Locate and identify every blood parasite.
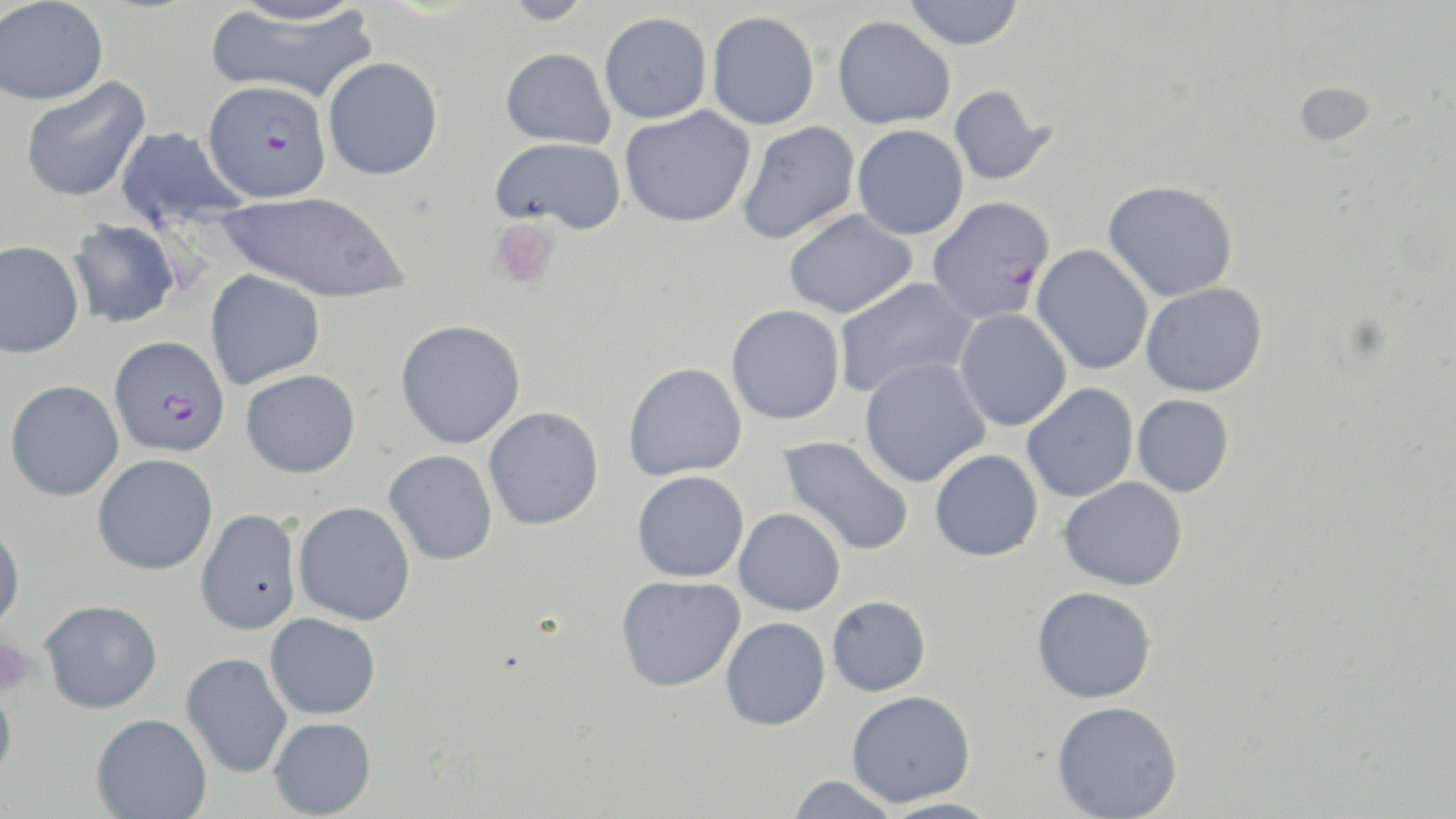
Approximate bounding boxes as named x1/y1/x2/y2 corners in pixels.
Plasmodium falciparum-infected red blood cells: (x1=203, y1=80, x2=332, y2=202), (x1=927, y1=196, x2=1056, y2=323), (x1=109, y1=335, x2=230, y2=456).
No Plasmodium ovale, Plasmodium malariae, Plasmodium vivax, Babesia divergens, or Trypanosoma brucei observed.

slide-level diagnosis = Plasmodium falciparum
platelet locations = approximate bounding boxes as named x1/y1/x2/y2 corners in pixels: (x1=488, y1=218, x2=561, y2=290), (x1=0, y1=637, x2=36, y2=701)
preparation = thin blood film
image size = 1456×819 pixels
field of view = single
modality = light microscopy
magnification = 1000x
uninfected red blood cell locations = approximate bounding boxes as named x1/y1/x2/y2 corners in pixels: (x1=500, y1=0, x2=598, y2=25), (x1=902, y1=0, x2=1025, y2=50), (x1=0, y1=1, x2=109, y2=106), (x1=225, y1=1, x2=372, y2=26), (x1=205, y1=4, x2=379, y2=104), (x1=707, y1=10, x2=820, y2=130), (x1=599, y1=12, x2=712, y2=124), (x1=832, y1=15, x2=956, y2=129), (x1=500, y1=48, x2=616, y2=148), (x1=322, y1=57, x2=443, y2=180), (x1=19, y1=76, x2=151, y2=203), (x1=1294, y1=82, x2=1375, y2=146), (x1=949, y1=84, x2=1054, y2=186), (x1=619, y1=105, x2=756, y2=228), (x1=736, y1=121, x2=860, y2=245), (x1=852, y1=124, x2=969, y2=241), (x1=114, y1=126, x2=247, y2=229), (x1=490, y1=136, x2=626, y2=233), (x1=1103, y1=180, x2=1239, y2=303), (x1=219, y1=190, x2=409, y2=303), (x1=783, y1=209, x2=918, y2=319), (x1=67, y1=219, x2=181, y2=329), (x1=0, y1=239, x2=84, y2=358), (x1=1031, y1=245, x2=1154, y2=375), (x1=205, y1=269, x2=326, y2=389), (x1=832, y1=276, x2=977, y2=399), (x1=1141, y1=282, x2=1267, y2=397), (x1=726, y1=304, x2=845, y2=425), (x1=954, y1=309, x2=1072, y2=432), (x1=395, y1=319, x2=526, y2=449), (x1=859, y1=357, x2=991, y2=487), (x1=622, y1=363, x2=748, y2=481), (x1=240, y1=369, x2=361, y2=478), (x1=4, y1=379, x2=124, y2=501), (x1=1021, y1=383, x2=1138, y2=502), (x1=1132, y1=395, x2=1234, y2=497), (x1=483, y1=406, x2=604, y2=530), (x1=779, y1=435, x2=915, y2=557), (x1=929, y1=448, x2=1043, y2=561), (x1=384, y1=449, x2=498, y2=565), (x1=93, y1=453, x2=218, y2=575), (x1=632, y1=470, x2=749, y2=583), (x1=1058, y1=476, x2=1188, y2=591), (x1=293, y1=501, x2=416, y2=625), (x1=733, y1=507, x2=846, y2=615), (x1=195, y1=508, x2=302, y2=635), (x1=0, y1=521, x2=25, y2=635), (x1=616, y1=574, x2=745, y2=692), (x1=1031, y1=585, x2=1157, y2=703), (x1=826, y1=595, x2=931, y2=696), (x1=39, y1=599, x2=162, y2=713), (x1=265, y1=613, x2=381, y2=719), (x1=720, y1=617, x2=831, y2=731), (x1=181, y1=652, x2=293, y2=778), (x1=0, y1=676, x2=18, y2=786), (x1=846, y1=690, x2=976, y2=808), (x1=1051, y1=700, x2=1183, y2=819), (x1=91, y1=713, x2=212, y2=819), (x1=268, y1=717, x2=377, y2=818), (x1=786, y1=775, x2=900, y2=817), (x1=875, y1=797, x2=1004, y2=819)
stain = May-Grünwald-Giemsa